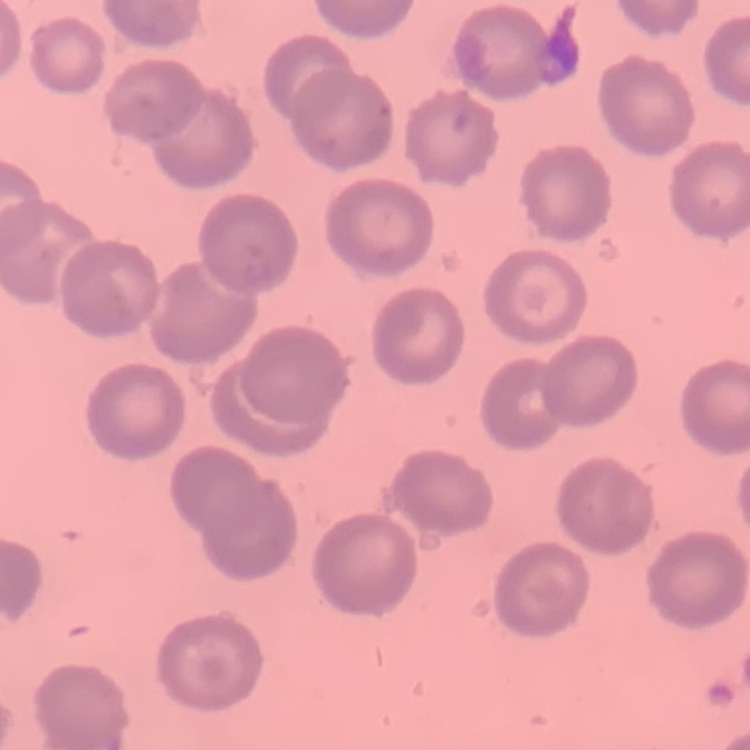
erythrocyte_morphology: no rouleaux formation
image_type: one tile cut from a larger photomicrograph
stain: Field's or Giemsa
preparation: thin peripheral smear